Outline each Plasmodium malariae-infected red blood cell.
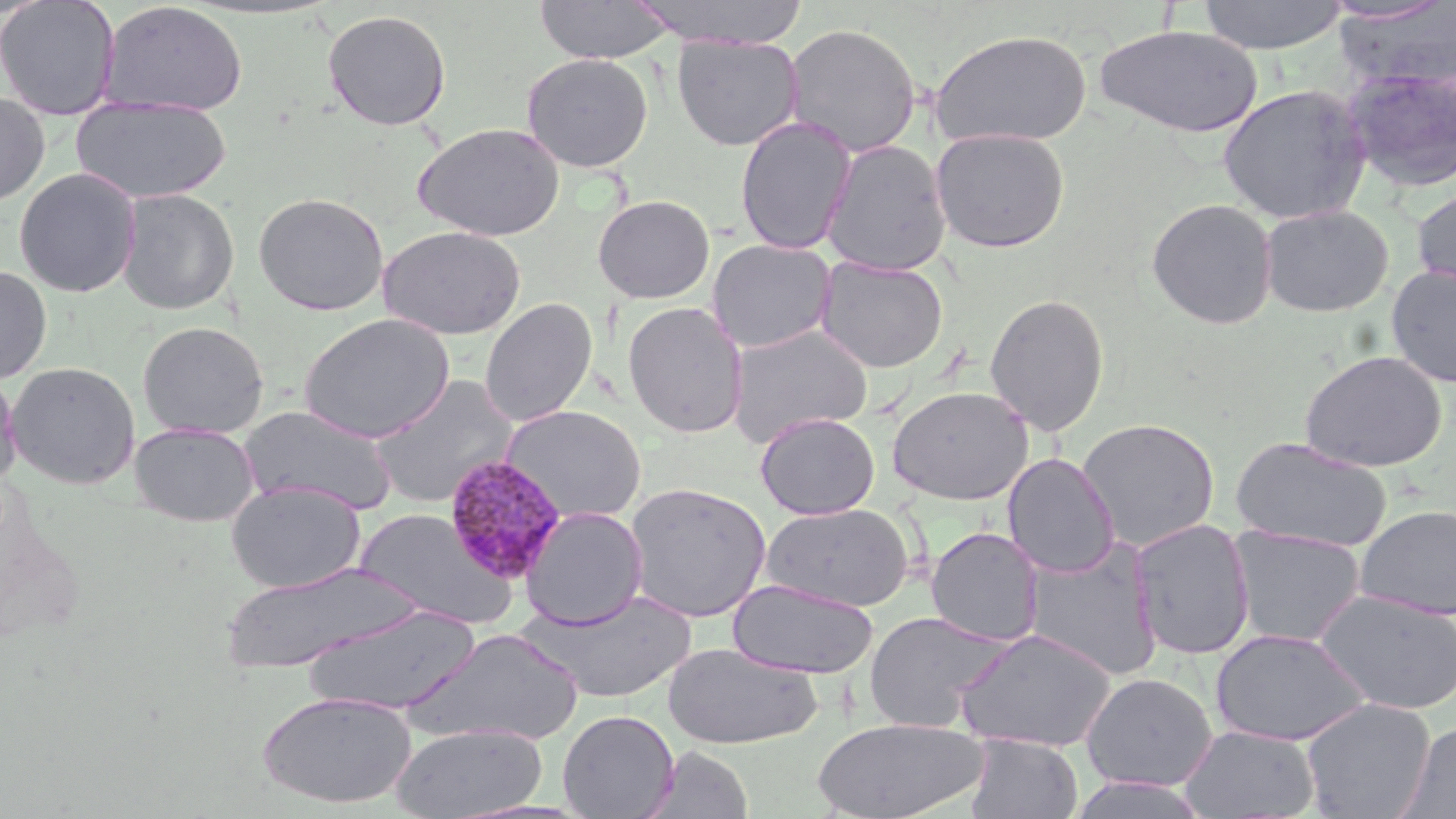

Approximate bounding boxes as (x1,y1)-(x2,y2) corner pairs in pixels.
Plasmodium malariae-infected red blood cells: (443,454)-(567,583).

Summary:
  - Uninfected red blood cell locations: (0,0)-(121,120), (533,0)-(675,64), (629,0)-(809,48), (1197,0)-(1350,54), (101,2)-(248,116), (1332,2)-(1456,92), (322,9)-(452,131), (783,22)-(922,158), (1094,24)-(1263,138), (929,28)-(1093,149), (672,35)-(804,151), (521,53)-(653,172), (1342,64)-(1456,193), (1217,83)-(1372,224), (0,91)-(50,208), (71,96)-(232,204), (734,116)-(857,255), (412,123)-(565,242), (931,128)-(1070,252), (821,140)-(951,276), (13,167)-(142,298), (1411,184)-(1456,298), (116,188)-(239,315), (253,191)-(389,316), (592,194)-(715,304), (1146,197)-(1279,330), (1259,204)-(1394,317), (378,225)-(526,340), (707,238)-(836,353), (817,256)-(948,372), (1386,263)-(1456,388), (0,264)-(52,384), (985,293)-(1110,436), (480,297)-(598,427), (622,302)-(748,438), (298,313)-(456,443), (136,321)-(270,439), (727,324)-(873,446), (1299,350)-(1447,472), (5,361)-(141,489), (0,368)-(22,489), (369,375)-(520,508), (887,386)-(1033,504), (238,405)-(398,514), (502,405)-(647,524), (755,412)-(879,519), (1078,417)-(1220,551), (129,422)-(260,527), (1230,437)-(1393,553), (1003,453)-(1119,578), (227,481)-(365,593), (624,482)-(771,622), (760,502)-(914,612), (1355,504)-(1456,621), (520,506)-(649,629), (354,508)-(515,629), (1130,518)-(1256,660), (1227,525)-(1366,648), (925,526)-(1045,647), (1024,538)-(1163,679), (218,560)-(420,674), (727,579)-(877,679), (526,588)-(697,704), (1314,588)-(1456,715), (302,605)-(481,716), (862,611)-(1009,733), (409,627)-(585,745), (1210,627)-(1370,746), (954,628)-(1116,752), (662,641)-(822,749), (1081,672)-(1217,791), (256,690)-(416,808), (1301,697)-(1436,819), (557,709)-(679,819), (810,716)-(989,819), (1395,721)-(1456,818), (391,722)-(546,818), (1180,725)-(1321,818), (964,734)-(1083,818), (643,746)-(754,819), (1063,774)-(1210,819)
  - Slide-level diagnosis: Plasmodium malariae
  - Preparation: thin blood film
  - Image size: 1456×819 pixels
  - Field of view: single
  - Magnification: 1000x
  - Stain: May-Grünwald-Giemsa
  - Modality: light microscopy